Locate every blood parasite and identify its species.
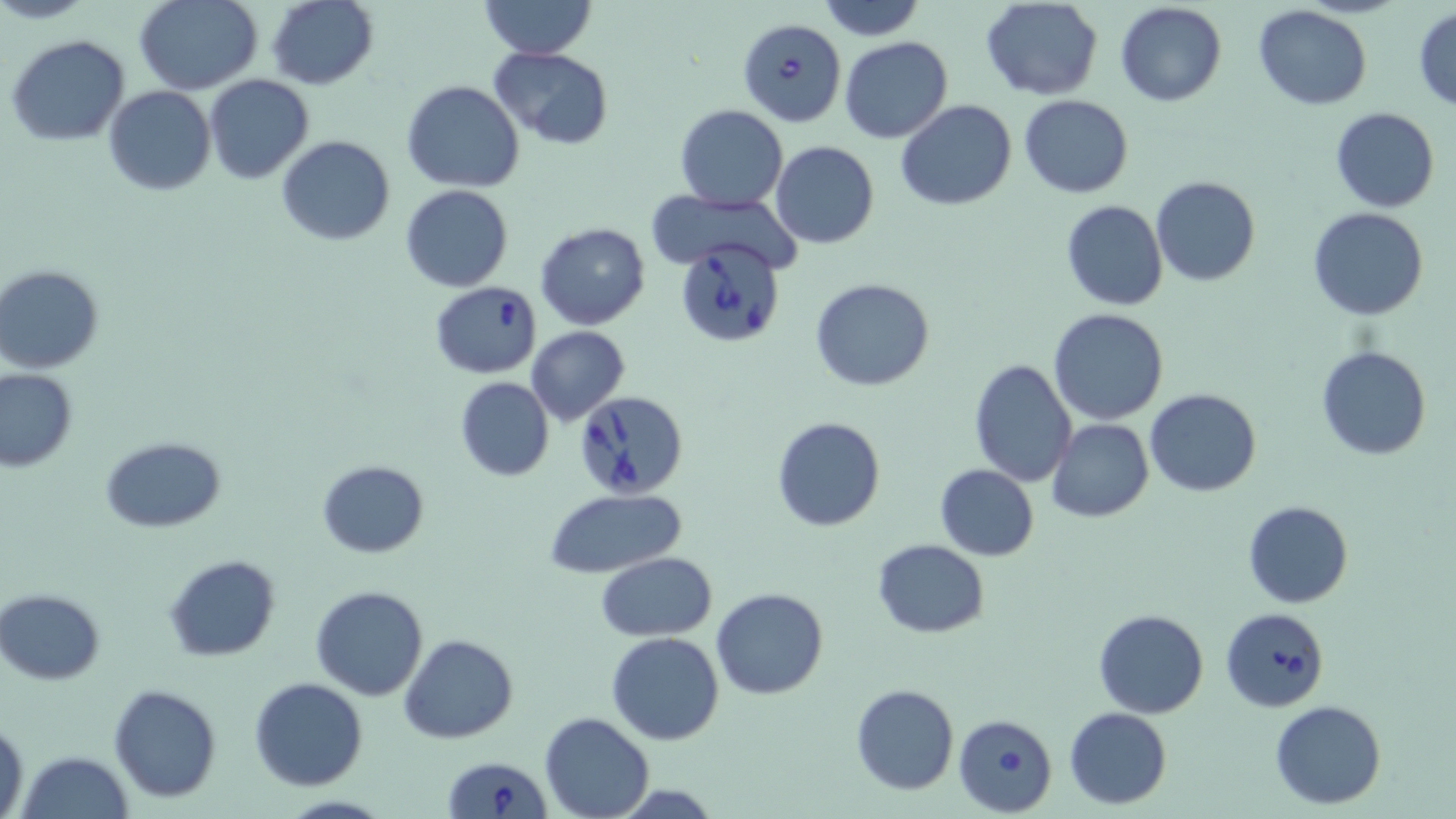

Approximate bounding boxes as named x1/y1/x2/y2 corners in pixels.
Babesia divergens-infected red blood cells: (x1=738, y1=17, x2=847, y2=127), (x1=677, y1=240, x2=783, y2=348), (x1=430, y1=282, x2=543, y2=378), (x1=576, y1=389, x2=689, y2=498), (x1=1220, y1=606, x2=1331, y2=714), (x1=954, y1=713, x2=1058, y2=816), (x1=443, y1=756, x2=549, y2=819).
No Plasmodium falciparum, Plasmodium ovale, Plasmodium malariae, Plasmodium vivax, or Trypanosoma brucei observed.

Uninfected red blood cell locations: (x1=3, y1=0, x2=98, y2=25), (x1=134, y1=0, x2=262, y2=93), (x1=267, y1=0, x2=378, y2=90), (x1=479, y1=0, x2=597, y2=61), (x1=816, y1=0, x2=927, y2=41), (x1=980, y1=0, x2=1102, y2=100), (x1=1114, y1=1, x2=1227, y2=108), (x1=1252, y1=5, x2=1372, y2=109), (x1=1412, y1=6, x2=1456, y2=111), (x1=6, y1=34, x2=129, y2=147), (x1=839, y1=37, x2=953, y2=144), (x1=490, y1=47, x2=615, y2=149), (x1=206, y1=74, x2=314, y2=186), (x1=402, y1=81, x2=525, y2=193), (x1=104, y1=86, x2=216, y2=196), (x1=1019, y1=94, x2=1134, y2=199), (x1=897, y1=101, x2=1017, y2=211), (x1=675, y1=105, x2=787, y2=211), (x1=1331, y1=107, x2=1439, y2=212), (x1=276, y1=135, x2=396, y2=245), (x1=771, y1=141, x2=879, y2=249), (x1=1151, y1=177, x2=1260, y2=288), (x1=399, y1=185, x2=514, y2=293), (x1=644, y1=185, x2=798, y2=272), (x1=1060, y1=200, x2=1169, y2=311), (x1=1307, y1=207, x2=1429, y2=320), (x1=535, y1=221, x2=650, y2=330), (x1=0, y1=265, x2=105, y2=373), (x1=810, y1=276, x2=935, y2=392), (x1=1048, y1=309, x2=1171, y2=426), (x1=526, y1=327, x2=630, y2=425), (x1=1315, y1=345, x2=1432, y2=462), (x1=968, y1=359, x2=1077, y2=486), (x1=1, y1=368, x2=78, y2=471), (x1=455, y1=376, x2=554, y2=481), (x1=1144, y1=389, x2=1263, y2=496), (x1=771, y1=415, x2=886, y2=533), (x1=1046, y1=418, x2=1155, y2=522), (x1=101, y1=435, x2=226, y2=532), (x1=317, y1=459, x2=430, y2=557), (x1=935, y1=465, x2=1039, y2=560), (x1=543, y1=488, x2=688, y2=579), (x1=1242, y1=501, x2=1354, y2=608), (x1=871, y1=538, x2=991, y2=637), (x1=596, y1=552, x2=718, y2=640), (x1=165, y1=554, x2=281, y2=660), (x1=311, y1=585, x2=428, y2=700), (x1=1, y1=588, x2=105, y2=685), (x1=711, y1=588, x2=828, y2=699), (x1=1093, y1=609, x2=1209, y2=719), (x1=607, y1=632, x2=725, y2=745), (x1=399, y1=634, x2=519, y2=744), (x1=248, y1=677, x2=370, y2=791), (x1=108, y1=683, x2=224, y2=802), (x1=850, y1=684, x2=960, y2=796), (x1=1270, y1=700, x2=1387, y2=810), (x1=1064, y1=706, x2=1172, y2=809), (x1=540, y1=712, x2=653, y2=819), (x1=1, y1=717, x2=28, y2=819), (x1=17, y1=750, x2=134, y2=819). Slide-level diagnosis: Babesia divergens. Thin blood smear. 1000x magnification. Single field of view. Optical microscopy. Image is 1456×819 pixels. May-Grünwald-Giemsa stain.